Outline each blood parasite and name the species.
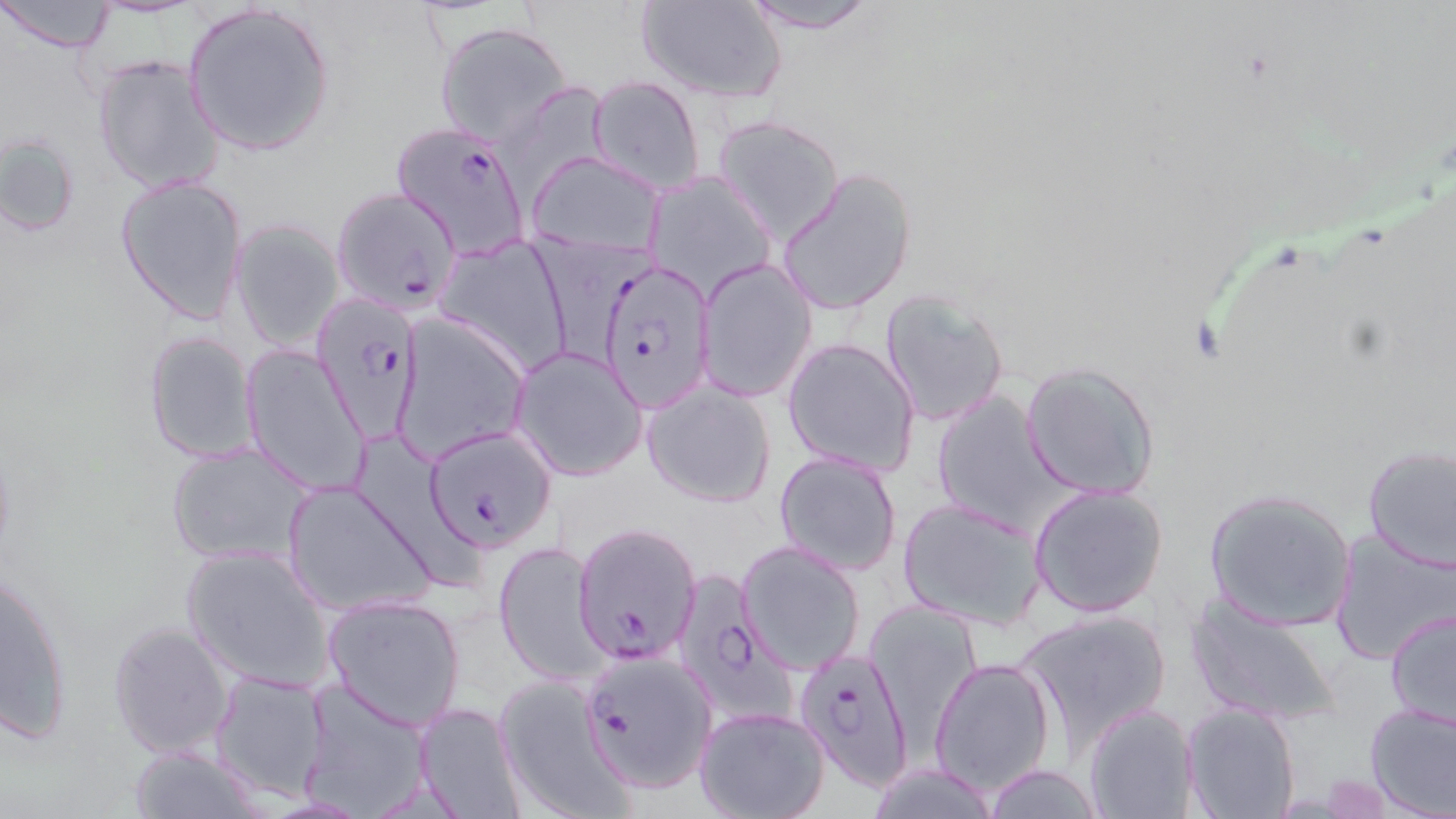

Approximate bounding boxes as named x1/y1/x2/y2 corners in pixels.
Plasmodium falciparum-infected red blood cells: (x1=392, y1=123, x2=533, y2=257), (x1=330, y1=186, x2=463, y2=314), (x1=596, y1=257, x2=716, y2=412), (x1=311, y1=289, x2=424, y2=441), (x1=426, y1=427, x2=558, y2=553), (x1=572, y1=522, x2=701, y2=665), (x1=675, y1=569, x2=794, y2=712), (x1=794, y1=647, x2=914, y2=791), (x1=587, y1=654, x2=721, y2=791).
No Plasmodium ovale, Plasmodium malariae, Plasmodium vivax, Babesia divergens, or Trypanosoma brucei observed.

{
  "slide_level_diagnosis": "Plasmodium falciparum",
  "preparation": "thin blood smear",
  "uninfected_red_blood_cell_locations": "approximate bounding boxes as named x1/y1/x2/y2 corners in pixels: (x1=0, y1=0, x2=117, y2=53), (x1=734, y1=0, x2=880, y2=34), (x1=637, y1=1, x2=786, y2=102), (x1=182, y1=3, x2=337, y2=157), (x1=434, y1=22, x2=573, y2=147), (x1=91, y1=55, x2=226, y2=195), (x1=588, y1=76, x2=707, y2=195), (x1=714, y1=115, x2=843, y2=244), (x1=1, y1=134, x2=81, y2=239), (x1=528, y1=152, x2=661, y2=255), (x1=777, y1=166, x2=918, y2=316), (x1=646, y1=173, x2=776, y2=300), (x1=115, y1=174, x2=248, y2=326), (x1=229, y1=220, x2=344, y2=349), (x1=435, y1=237, x2=574, y2=375), (x1=697, y1=259, x2=816, y2=402), (x1=879, y1=290, x2=1010, y2=429), (x1=392, y1=315, x2=528, y2=464), (x1=142, y1=331, x2=260, y2=462), (x1=782, y1=337, x2=919, y2=476), (x1=240, y1=342, x2=370, y2=497), (x1=511, y1=347, x2=648, y2=482), (x1=1020, y1=360, x2=1161, y2=500), (x1=643, y1=381, x2=776, y2=508), (x1=930, y1=389, x2=1069, y2=531), (x1=166, y1=443, x2=317, y2=566), (x1=1361, y1=443, x2=1456, y2=571), (x1=370, y1=445, x2=477, y2=591), (x1=774, y1=451, x2=902, y2=577), (x1=281, y1=479, x2=437, y2=617), (x1=1027, y1=482, x2=1170, y2=619), (x1=1202, y1=487, x2=1359, y2=632), (x1=897, y1=497, x2=1045, y2=630), (x1=1330, y1=532, x2=1455, y2=664), (x1=495, y1=539, x2=604, y2=685), (x1=737, y1=541, x2=866, y2=676), (x1=182, y1=543, x2=336, y2=692), (x1=3, y1=565, x2=74, y2=742), (x1=320, y1=593, x2=467, y2=731), (x1=1184, y1=594, x2=1340, y2=728), (x1=867, y1=603, x2=979, y2=735), (x1=1385, y1=607, x2=1456, y2=734), (x1=1018, y1=608, x2=1172, y2=752), (x1=106, y1=620, x2=236, y2=759), (x1=930, y1=657, x2=1055, y2=795), (x1=210, y1=670, x2=331, y2=800), (x1=492, y1=675, x2=635, y2=818), (x1=298, y1=681, x2=434, y2=817), (x1=412, y1=701, x2=527, y2=819), (x1=1183, y1=701, x2=1300, y2=819), (x1=1364, y1=702, x2=1456, y2=817), (x1=1084, y1=703, x2=1199, y2=818), (x1=695, y1=706, x2=829, y2=819), (x1=129, y1=745, x2=262, y2=818), (x1=980, y1=763, x2=1107, y2=819), (x1=864, y1=764, x2=1000, y2=817)",
  "field_of_view": "single",
  "image_size": "1456×819 pixels",
  "magnification": "1000x",
  "modality": "light microscopy",
  "stain": "May-Grünwald-Giemsa"
}